Name the parasite shown.
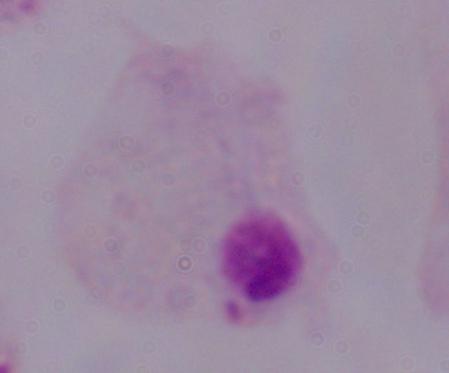
A trichomonad.

modality = photomicrograph
magnification = 1000x